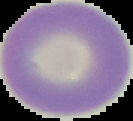 Image is 133×121 pixels. Cell region segmented out of the field of view; the surrounding area is masked to black. Malaria status: uninfected. From a thin blood smear.